State which parasite is depicted.
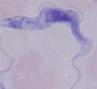
This is a trypanosome.

Summary:
  - Magnification: 1000x
  - Modality: micrograph